Look for Plasmodium parasites.
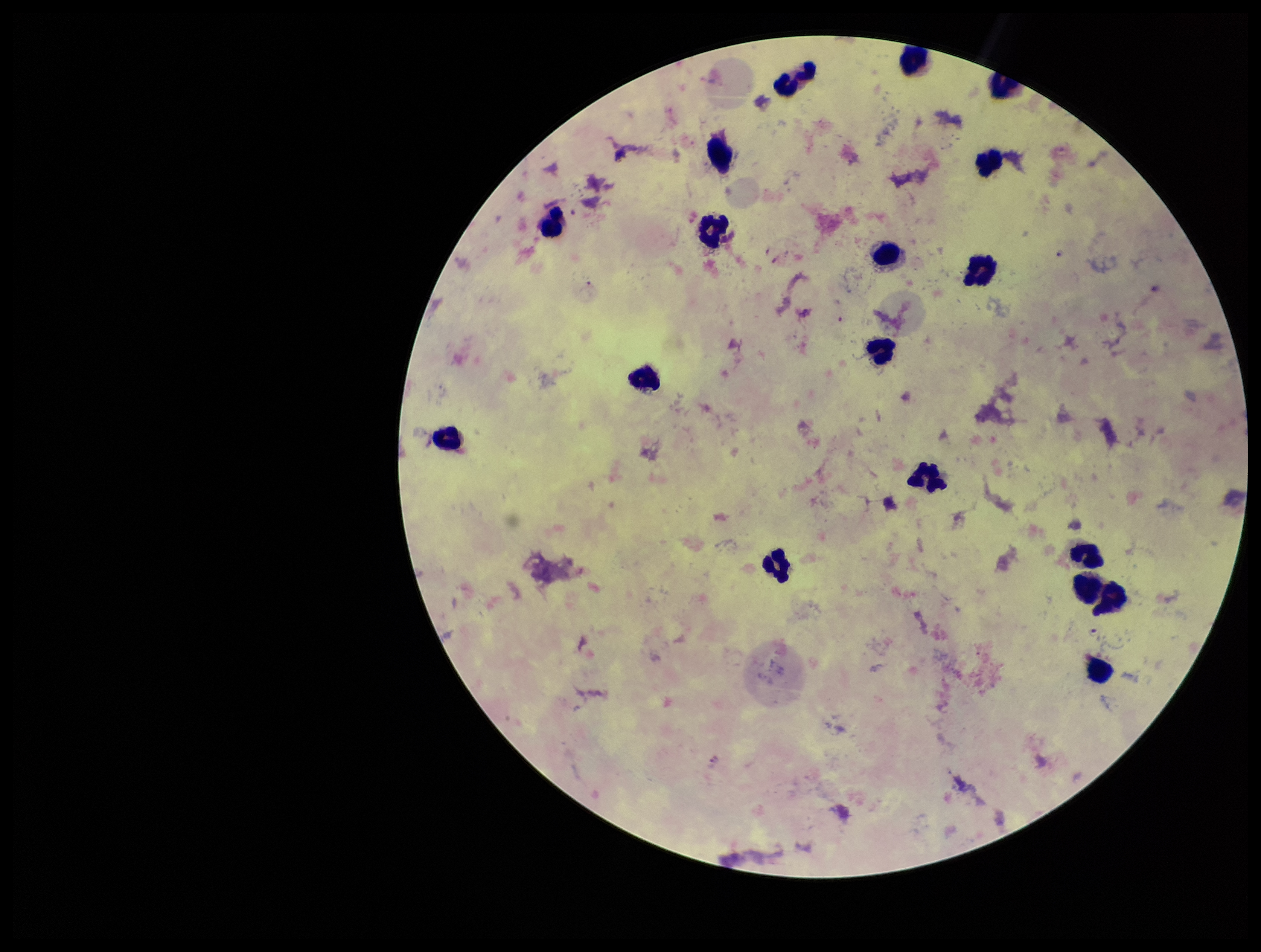
Identified.

Summary:
  - Species reported for this patient: Plasmodium falciparum
  - Leukocyte count: 17
  - Field of view: single
  - Capture: smartphone photograph through the microscope eyepiece
  - Parasite count: 2
  - Image size: 1261×952 pixels
  - Stain: Giemsa
  - Preparation: thick smear
  - Patient malaria status: positive